Point out each malaria parasite.
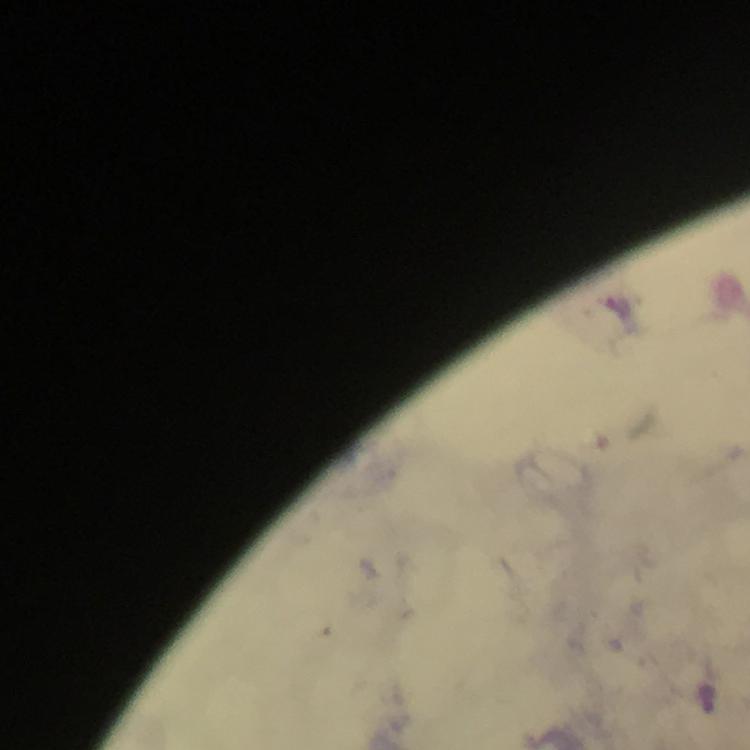
Approximate object centers, in pixels from the top-left corner.
Malaria parasites: (x=708, y=698).

immersion oil = applied
capture = smartphone camera through the microscope
preparation = thick blood smear
cropped from = a single field of view
stain = Giemsa
image size = 750×750 pixels
magnification = 100x
context = from a malaria diagnostic workup